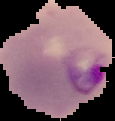
Summary:
  - Image size: 115×121 pixels
  - Image type: segmented cell region on a black background
  - Result: Plasmodium parasites detected
  - Preparation: thin blood smear